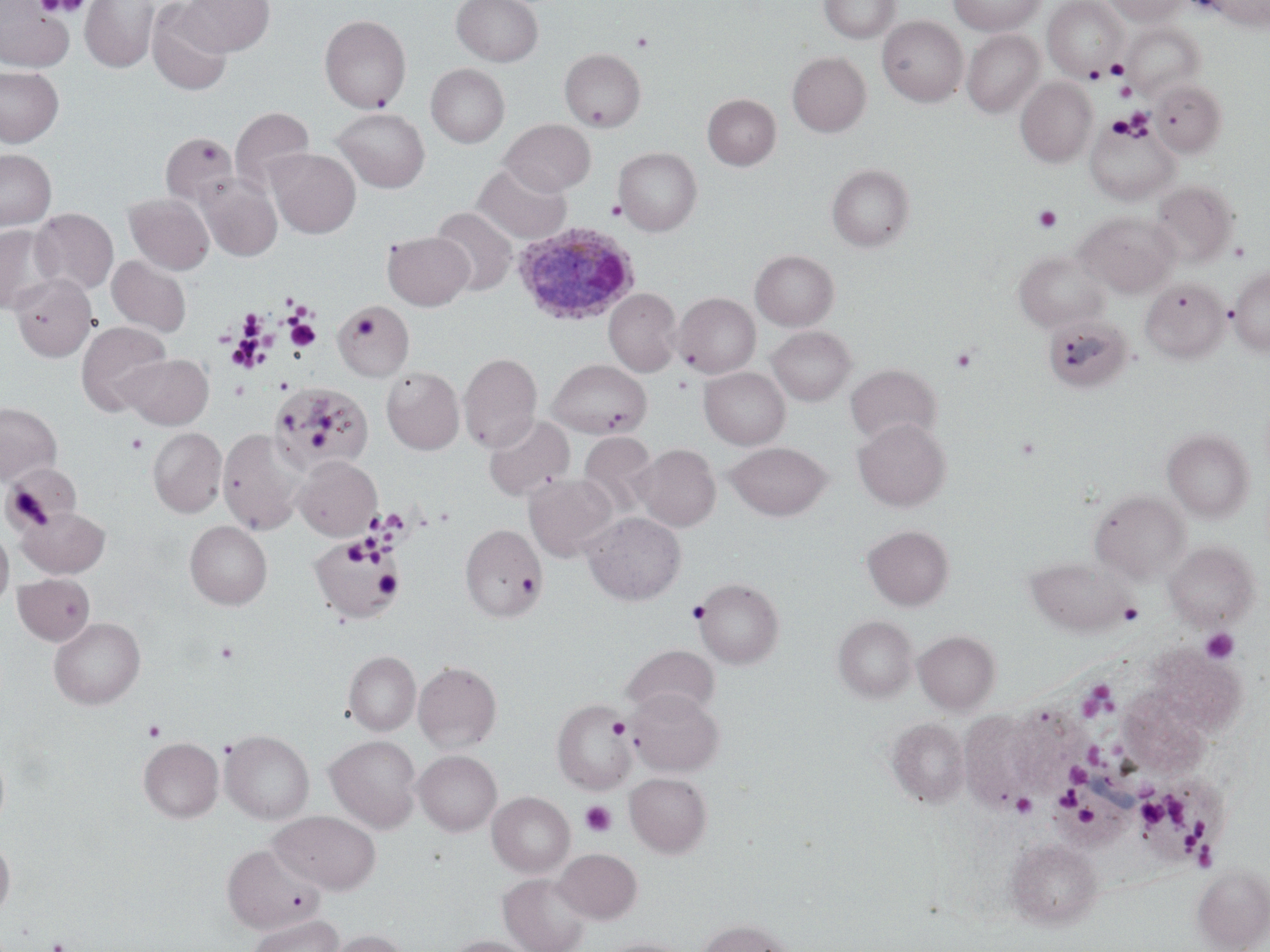

{
  "slide_level_diagnosis": "Plasmodium ovale",
  "stain": "May-Grünwald-Giemsa",
  "preparation": "thin blood film",
  "image_size": "1270×952 pixels",
  "field_of_view": "single",
  "modality": "optical microscopy",
  "uninfected_red_blood_cell_locations": "approximate bounding boxes as (x1, y1, x2, y2) in pixels: (80, 0, 158, 71), (182, 0, 274, 56), (452, 0, 542, 66), (819, 0, 900, 43), (947, 0, 1046, 35), (1103, 0, 1187, 25), (1207, 0, 1270, 30), (0, 1, 73, 72), (1043, 1, 1127, 81), (147, 2, 232, 96), (320, 15, 410, 112), (877, 16, 968, 106), (1124, 23, 1205, 99), (962, 30, 1044, 117), (560, 48, 645, 131), (787, 51, 871, 136), (426, 63, 509, 147), (0, 65, 64, 147), (1016, 78, 1096, 166), (1150, 79, 1227, 158), (703, 94, 780, 169), (231, 107, 315, 191), (332, 108, 429, 192), (1086, 118, 1180, 204), (500, 119, 595, 196), (161, 132, 239, 208), (267, 148, 360, 238), (614, 148, 701, 235), (0, 149, 56, 229), (472, 163, 571, 244), (827, 164, 915, 251), (197, 175, 282, 261), (1151, 181, 1238, 266), (124, 193, 214, 274), (431, 207, 517, 295), (30, 208, 118, 294), (1077, 212, 1179, 296), (0, 225, 60, 314), (383, 231, 474, 310), (751, 250, 838, 330), (1014, 250, 1107, 332), (107, 256, 192, 337), (1227, 266, 1270, 356), (10, 273, 97, 362), (1140, 278, 1229, 362), (604, 288, 682, 376), (674, 293, 760, 378), (335, 300, 415, 380), (1042, 314, 1133, 394), (76, 321, 172, 416), (768, 326, 855, 405), (459, 352, 542, 452), (123, 354, 213, 429), (547, 359, 651, 438), (846, 364, 940, 445), (382, 366, 464, 454), (699, 367, 789, 449), (270, 383, 373, 473), (0, 403, 61, 483), (483, 415, 574, 501), (853, 418, 949, 511), (148, 428, 227, 517), (218, 428, 307, 534), (1163, 429, 1253, 522), (579, 432, 658, 515), (725, 442, 832, 520), (633, 444, 720, 531), (294, 455, 382, 540), (1, 463, 76, 534), (524, 473, 617, 561), (1090, 490, 1189, 582), (18, 506, 110, 578), (582, 512, 686, 605), (185, 521, 272, 609), (461, 524, 546, 622), (862, 524, 953, 609), (0, 525, 14, 610), (310, 536, 404, 622), (1165, 540, 1258, 631), (1026, 556, 1130, 636), (13, 573, 95, 645), (693, 577, 784, 668), (834, 616, 917, 702), (49, 617, 145, 709), (914, 630, 1000, 714), (622, 645, 719, 718), (1153, 645, 1246, 734), (343, 651, 420, 735), (413, 661, 501, 753), (627, 688, 723, 776), (1119, 688, 1208, 773), (552, 699, 635, 795), (1008, 707, 1086, 780), (960, 710, 1036, 801), (886, 717, 970, 808), (220, 730, 314, 824), (326, 735, 421, 832), (139, 737, 224, 822), (414, 750, 501, 835), (1058, 757, 1145, 853), (625, 772, 712, 857), (1147, 772, 1227, 864), (487, 792, 574, 877), (270, 809, 381, 894), (0, 836, 15, 920), (1006, 838, 1101, 928), (222, 843, 325, 934), (554, 848, 642, 923), (1192, 865, 1270, 951), (498, 872, 591, 952), (245, 915, 344, 952), (696, 918, 794, 952), (326, 929, 409, 952), (442, 936, 536, 952), (599, 938, 693, 952)",
  "magnification": "1000x",
  "plasmodium_ovale_infected_red_blood_cell_locations": "approximate bounding boxes as (x1, y1, x2, y2) in pixels: (512, 222, 642, 324)",
  "platelet_locations": "approximate bounding boxes as (x1, y1, x2, y2) in pixels: (40, 0, 91, 18), (631, 33, 653, 53), (1105, 58, 1129, 79), (1084, 64, 1106, 83), (1115, 81, 1137, 101), (1125, 106, 1152, 133), (1106, 115, 1133, 138), (606, 200, 626, 219), (1034, 206, 1062, 232), (238, 309, 266, 338), (353, 310, 382, 341), (285, 319, 321, 351), (951, 346, 979, 374), (309, 428, 330, 448), (125, 432, 148, 455), (1014, 435, 1041, 461), (5, 484, 53, 530), (433, 507, 455, 526), (343, 538, 373, 564), (374, 569, 401, 597), (687, 600, 711, 624), (1118, 603, 1144, 625), (1200, 628, 1239, 664), (215, 640, 239, 664), (1079, 683, 1117, 719), (608, 718, 629, 739), (143, 720, 166, 741), (1086, 744, 1110, 770), (1066, 763, 1090, 785), (1053, 786, 1082, 809), (1011, 792, 1037, 818), (1164, 793, 1190, 828), (1138, 799, 1167, 827), (580, 801, 616, 837), (1077, 808, 1098, 827), (1184, 819, 1210, 853), (1197, 846, 1218, 871), (45, 939, 71, 952)"
}